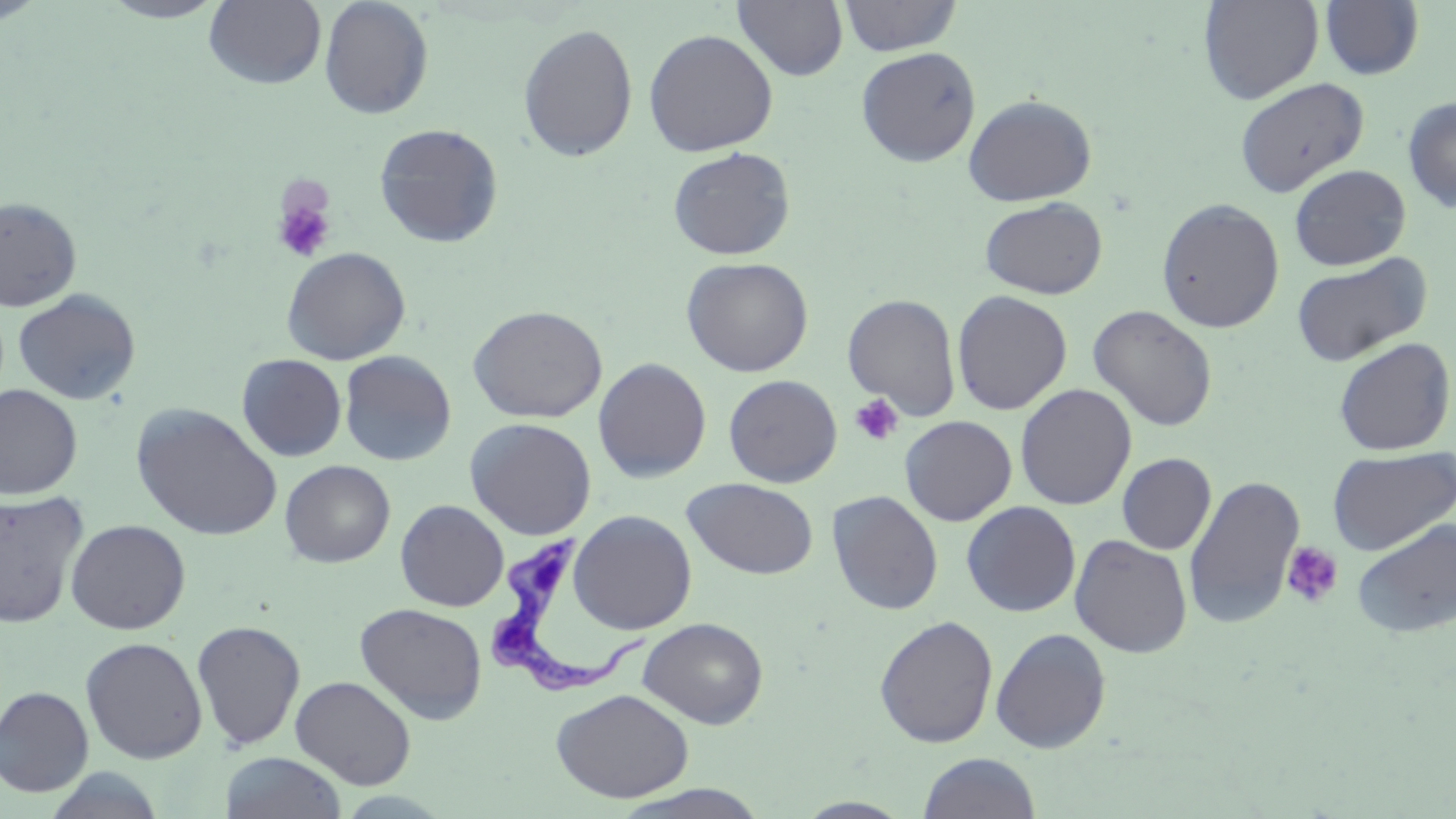

Summary:
  - Coordinate format: approximate bounding boxes as [x1, y1, x2, y2] in pixels
  - Uninfected red blood cell locations: [0, 0, 48, 25], [97, 0, 230, 23], [203, 0, 327, 90], [318, 0, 434, 119], [733, 0, 848, 81], [837, 0, 963, 57], [1199, 0, 1324, 104], [1320, 1, 1424, 80], [517, 23, 638, 162], [643, 28, 778, 157], [856, 46, 981, 167], [1234, 77, 1369, 198], [963, 94, 1096, 206], [1402, 95, 1456, 213], [374, 123, 504, 248], [667, 146, 796, 261], [1288, 164, 1411, 270], [979, 196, 1108, 299], [0, 197, 82, 313], [1156, 197, 1285, 333], [281, 247, 411, 365], [1291, 253, 1431, 366], [681, 256, 813, 377], [13, 289, 141, 405], [952, 290, 1072, 416], [842, 294, 961, 419], [467, 304, 607, 423], [1088, 304, 1218, 432], [1333, 336, 1455, 456], [339, 350, 456, 466], [237, 354, 347, 461], [592, 357, 712, 483], [723, 374, 843, 488], [1015, 383, 1137, 510], [0, 384, 83, 499], [131, 403, 282, 542], [900, 415, 1017, 526], [464, 417, 597, 539], [1327, 446, 1455, 555], [1117, 453, 1216, 554], [280, 460, 395, 568], [1183, 475, 1305, 629], [682, 478, 818, 579], [0, 490, 89, 630], [827, 490, 943, 615], [395, 499, 509, 612], [961, 501, 1081, 617], [568, 510, 697, 634], [1352, 518, 1456, 638], [65, 519, 191, 634], [1070, 534, 1193, 657], [355, 602, 487, 724], [874, 615, 998, 748], [638, 617, 768, 729], [191, 620, 306, 751], [991, 627, 1111, 752], [80, 636, 208, 763], [290, 675, 416, 790], [0, 686, 94, 796], [550, 688, 695, 803], [219, 751, 347, 819], [917, 752, 1041, 818], [39, 767, 170, 819], [610, 785, 771, 818]
  - Platelet locations: [271, 191, 336, 264], [849, 394, 903, 446], [1281, 541, 1344, 608]
  - Trypanosoma brucei locations: [480, 533, 649, 698]
  - Slide-level diagnosis: Trypanosoma brucei
  - Modality: light microscopy
  - Image size: 1456×819 pixels
  - Field of view: single
  - Preparation: thin blood film
  - Magnification: 1000x
  - Stain: May-Grünwald-Giemsa